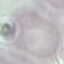

Malaria status: uninfected. Automatically extracted cell patch, resized to 64 × 64 pixels. Giemsa-stained preparation. Thin blood film. Photographed with a smartphone camera at the microscope eyepiece.